Point out each malaria parasite.
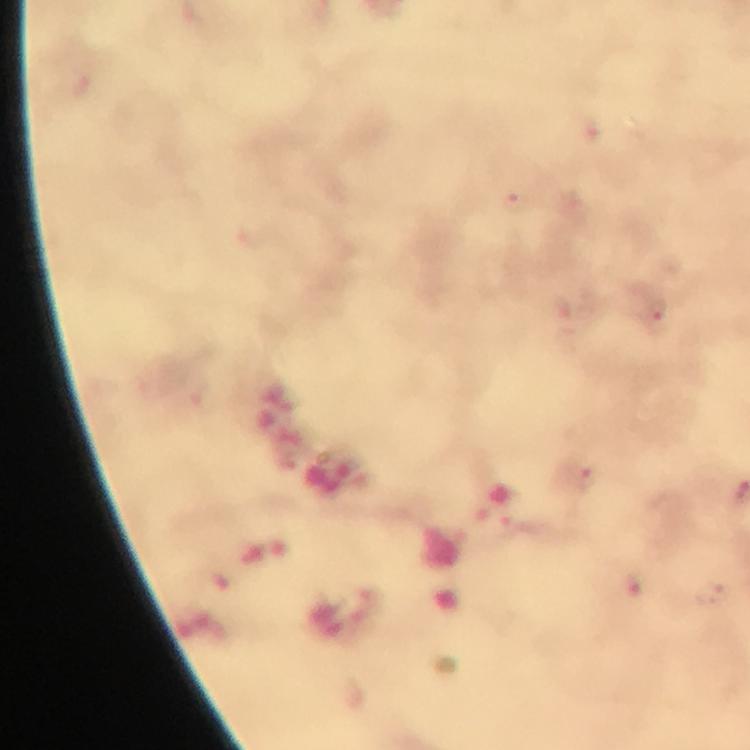
Approximate centers as (x, y) in pixels.
Malaria parasites: (516, 203), (656, 322), (585, 476), (634, 591).

cropped from = one field of view
capture = smartphone camera through the microscope
context = from a diagnostic examination for malaria
stain = Giemsa
preparation = thick blood film
magnification = 100x
immersion oil = used
image size = 750×750 pixels